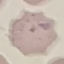

{
  "result": "negative for malaria parasites",
  "capture": "smartphone camera at the microscope eyepiece",
  "preparation": "thin blood film",
  "stain": "Giemsa",
  "image_type": "cell patch, automatically extracted from a larger field of view and resized to 64 × 64 pixels"
}